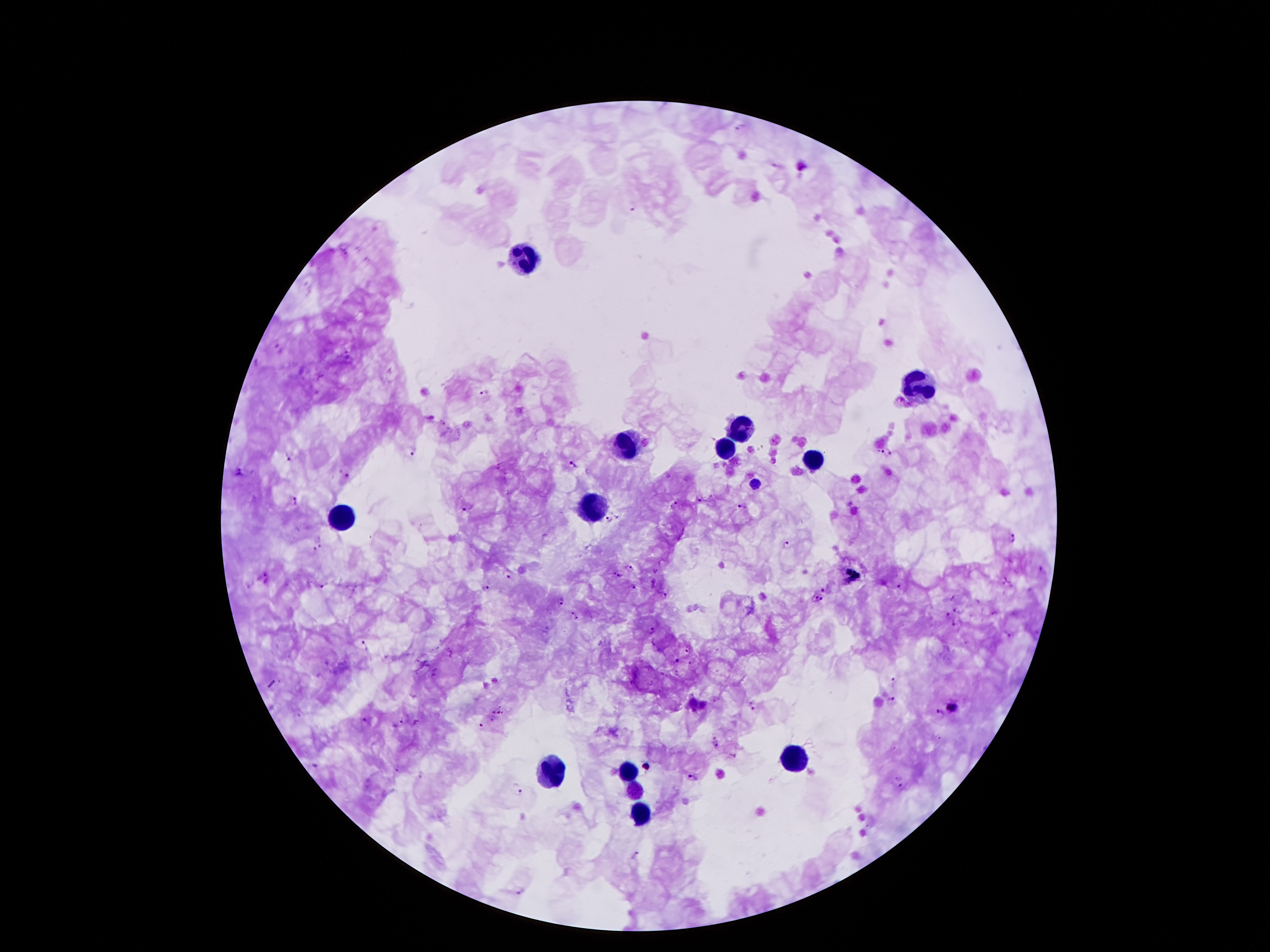 Approximate centers as (x, y) in pixels. Plasmodium parasite locations: (741, 126), (635, 207), (345, 252), (279, 348), (484, 393), (412, 452), (887, 452), (292, 459), (575, 464), (239, 472), (348, 475), (756, 483), (295, 500), (701, 500), (674, 505), (743, 505), (470, 506), (609, 519), (1013, 539), (322, 541), (784, 543), (313, 551), (630, 567), (1041, 569), (505, 573), (617, 575), (266, 578), (633, 586), (899, 586), (485, 588), (823, 590), (663, 595), (818, 599), (561, 600), (957, 609), (575, 614), (948, 616), (953, 623), (651, 630), (1009, 634), (368, 644), (688, 650), (677, 660), (692, 662), (677, 672), (894, 684), (891, 700), (717, 701), (753, 705), (953, 705), (501, 707), (493, 713), (498, 713), (502, 713), (940, 714), (365, 719), (492, 720), (402, 721), (480, 726), (716, 744), (735, 755), (397, 772), (422, 774), (693, 778), (896, 778), (516, 787), (904, 787), (636, 855), (519, 892). Leukocyte locations: (524, 255), (923, 385), (743, 430), (625, 444), (726, 449), (812, 461), (596, 507), (344, 520), (792, 753), (627, 770), (549, 776), (633, 791), (641, 810). Giemsa stain. Thick blood smear. Image is 1270×952 pixels. Photographed through the microscope eyepiece with a smartphone camera. Single field of view. 100x magnification. Patient malaria status: positive for Plasmodium falciparum.